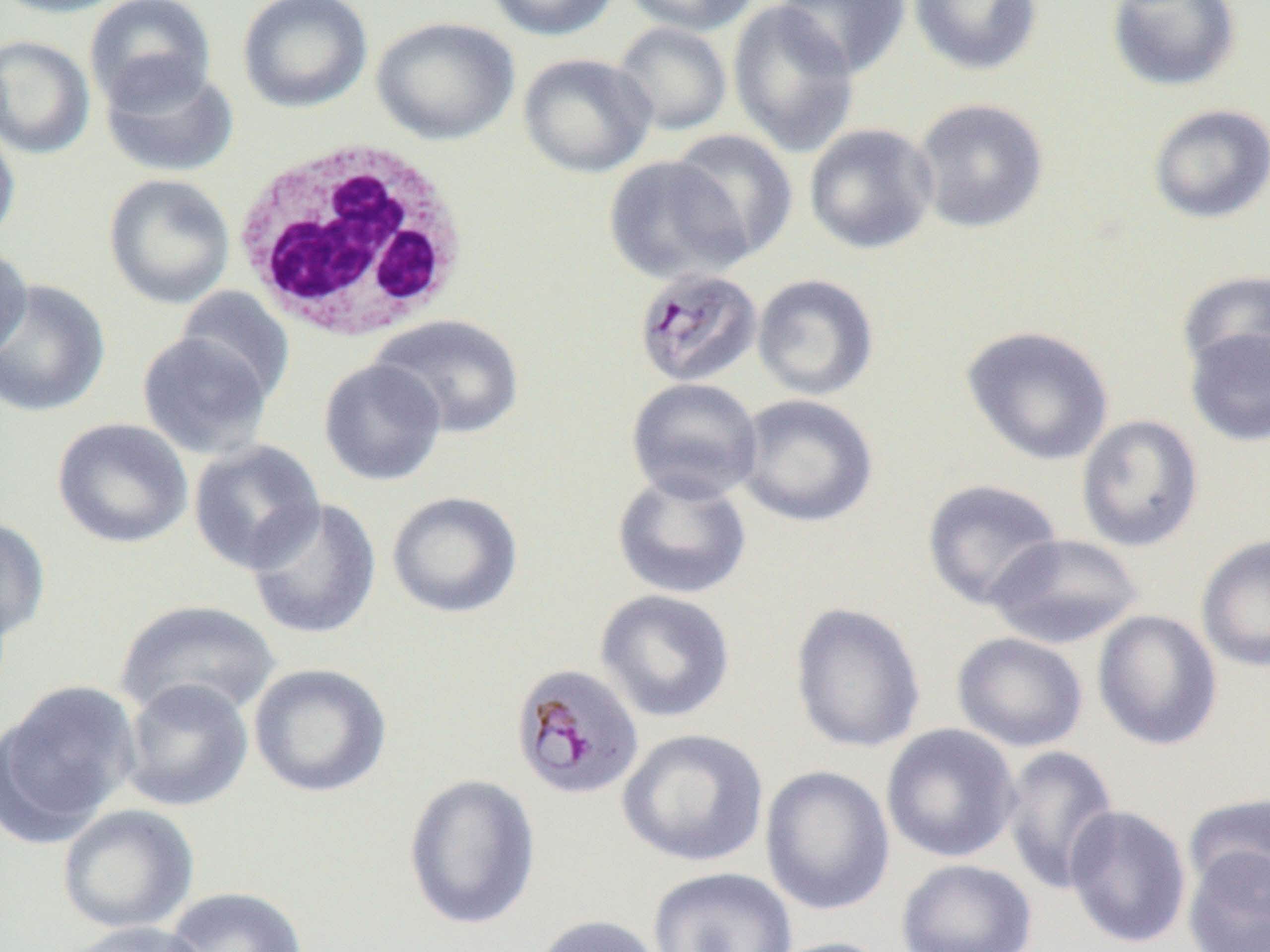

Summary:
  - Coordinate format: approximate bounding boxes as named x1/y1/x2/y2 corners in pixels
  - White blood cell locations: (x1=233, y1=139, x2=471, y2=343)
  - Uninfected red blood cell locations: (x1=0, y1=0, x2=135, y2=19), (x1=83, y1=0, x2=217, y2=113), (x1=238, y1=0, x2=373, y2=113), (x1=484, y1=0, x2=622, y2=42), (x1=621, y1=0, x2=762, y2=36), (x1=775, y1=0, x2=911, y2=79), (x1=908, y1=0, x2=1043, y2=77), (x1=1106, y1=0, x2=1242, y2=93), (x1=727, y1=1, x2=861, y2=158), (x1=370, y1=16, x2=520, y2=146), (x1=611, y1=21, x2=733, y2=137), (x1=0, y1=35, x2=95, y2=159), (x1=517, y1=52, x2=657, y2=178), (x1=99, y1=58, x2=239, y2=178), (x1=911, y1=97, x2=1050, y2=233), (x1=1148, y1=103, x2=1270, y2=224), (x1=0, y1=120, x2=21, y2=250), (x1=803, y1=123, x2=939, y2=255), (x1=665, y1=129, x2=798, y2=263), (x1=602, y1=155, x2=751, y2=286), (x1=102, y1=173, x2=236, y2=310), (x1=0, y1=244, x2=33, y2=365), (x1=1176, y1=269, x2=1270, y2=380), (x1=751, y1=273, x2=879, y2=401), (x1=0, y1=278, x2=111, y2=418), (x1=174, y1=286, x2=295, y2=407), (x1=369, y1=314, x2=524, y2=439), (x1=960, y1=325, x2=1114, y2=466), (x1=1185, y1=327, x2=1270, y2=447), (x1=137, y1=331, x2=273, y2=461), (x1=318, y1=358, x2=447, y2=487), (x1=626, y1=377, x2=763, y2=504), (x1=735, y1=393, x2=879, y2=528), (x1=1075, y1=413, x2=1204, y2=552), (x1=52, y1=417, x2=193, y2=549), (x1=187, y1=439, x2=325, y2=574), (x1=611, y1=470, x2=752, y2=600), (x1=921, y1=478, x2=1064, y2=610), (x1=385, y1=490, x2=523, y2=619), (x1=245, y1=496, x2=382, y2=641), (x1=0, y1=515, x2=52, y2=643), (x1=986, y1=533, x2=1145, y2=649), (x1=1196, y1=534, x2=1270, y2=673), (x1=594, y1=589, x2=736, y2=724), (x1=113, y1=598, x2=281, y2=723), (x1=790, y1=601, x2=926, y2=754), (x1=1092, y1=609, x2=1222, y2=750), (x1=951, y1=631, x2=1089, y2=752), (x1=248, y1=662, x2=392, y2=798), (x1=117, y1=677, x2=254, y2=812), (x1=0, y1=680, x2=141, y2=842), (x1=880, y1=724, x2=1021, y2=864), (x1=617, y1=727, x2=769, y2=867), (x1=1000, y1=745, x2=1120, y2=895), (x1=760, y1=765, x2=895, y2=916), (x1=402, y1=773, x2=541, y2=931), (x1=1184, y1=792, x2=1270, y2=904), (x1=56, y1=803, x2=200, y2=935), (x1=1064, y1=804, x2=1192, y2=949), (x1=1183, y1=845, x2=1270, y2=952), (x1=895, y1=858, x2=1038, y2=952), (x1=648, y1=866, x2=798, y2=952), (x1=162, y1=885, x2=308, y2=952), (x1=529, y1=914, x2=666, y2=952), (x1=61, y1=920, x2=210, y2=952), (x1=761, y1=936, x2=895, y2=952)
  - Plasmodium malariae-infected red blood cell locations: (x1=633, y1=266, x2=763, y2=388), (x1=510, y1=662, x2=644, y2=801)
  - Slide-level diagnosis: Plasmodium malariae
  - Magnification: 1000x
  - Preparation: thin blood film
  - Field of view: one of a larger specimen
  - Image size: 1270×952 pixels
  - Modality: optical microscopy